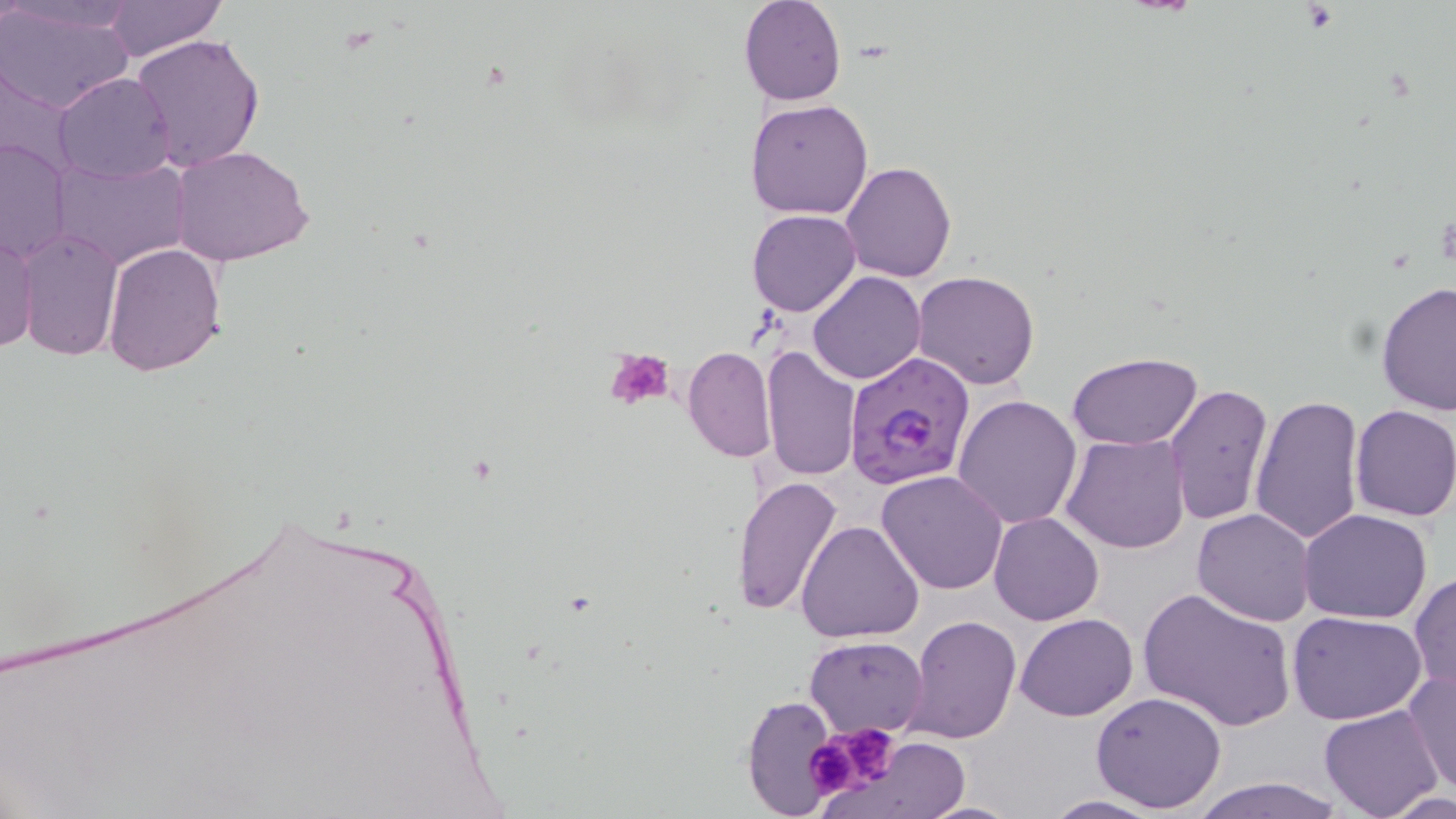

Summary:
  - Coordinate format: approximate bounding boxes as [x1, y1, x2, y2] in pixels
  - Uninfected red blood cell locations: [6, 0, 139, 36], [103, 0, 226, 61], [738, 0, 845, 106], [0, 3, 134, 115], [130, 33, 265, 172], [54, 72, 175, 184], [746, 99, 874, 221], [0, 137, 73, 265], [170, 144, 315, 267], [50, 155, 191, 272], [842, 161, 956, 283], [746, 209, 861, 316], [0, 228, 38, 357], [13, 228, 124, 361], [102, 241, 227, 376], [807, 272, 924, 385], [912, 272, 1040, 391], [1377, 281, 1456, 417], [760, 346, 861, 484], [682, 347, 778, 463], [1067, 352, 1203, 451], [1163, 382, 1276, 527], [952, 394, 1082, 529], [1249, 395, 1364, 548], [1349, 404, 1456, 522], [1060, 434, 1189, 554], [876, 471, 1008, 594], [731, 475, 843, 618], [1299, 508, 1432, 624], [1192, 509, 1317, 626], [989, 512, 1104, 625], [796, 519, 924, 643], [1410, 573, 1455, 693], [1139, 587, 1297, 732], [1287, 611, 1428, 726], [1015, 613, 1139, 720], [906, 615, 1022, 744], [805, 635, 929, 737], [1402, 668, 1456, 796], [1090, 692, 1226, 812], [741, 693, 838, 817], [1319, 705, 1444, 819], [866, 737, 969, 816], [1190, 774, 1343, 817], [1385, 788, 1455, 818], [1041, 794, 1170, 818], [921, 799, 1021, 818]
  - Platelet locations: [604, 347, 678, 411], [818, 722, 905, 795], [804, 733, 870, 801]
  - Plasmodium falciparum-infected red blood cell locations: [845, 352, 973, 490]
  - Slide-level diagnosis: Plasmodium falciparum
  - Image size: 1456×819 pixels
  - Magnification: 1000x
  - Preparation: thin blood smear
  - Field of view: single
  - Stain: May-Grünwald-Giemsa
  - Modality: light microscopy